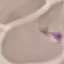
{
  "result": "negative for malaria parasites",
  "capture": "smartphone camera at the microscope eyepiece",
  "preparation": "thin smear",
  "image_type": "cell patch, automatically extracted from a larger field of view and resized to 64 × 64 pixels",
  "stain": "Giemsa"
}